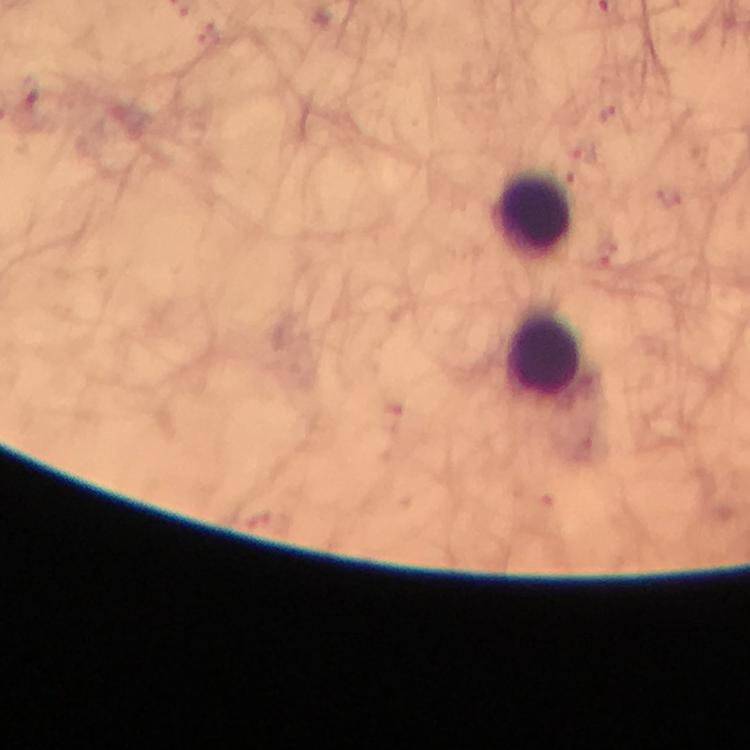 Approximate centers as {x, y} in pixels. Leukocyte locations: {531, 214}, {544, 356}. Smartphone photograph taken through a microscope. Plasmodium parasites: none detected. Giemsa-stained preparation. Immersion oil was used. Thick blood smear. At 100x magnification. From a diagnostic examination for malaria. Cropped region of a single field of view. Image is 750×750 pixels.